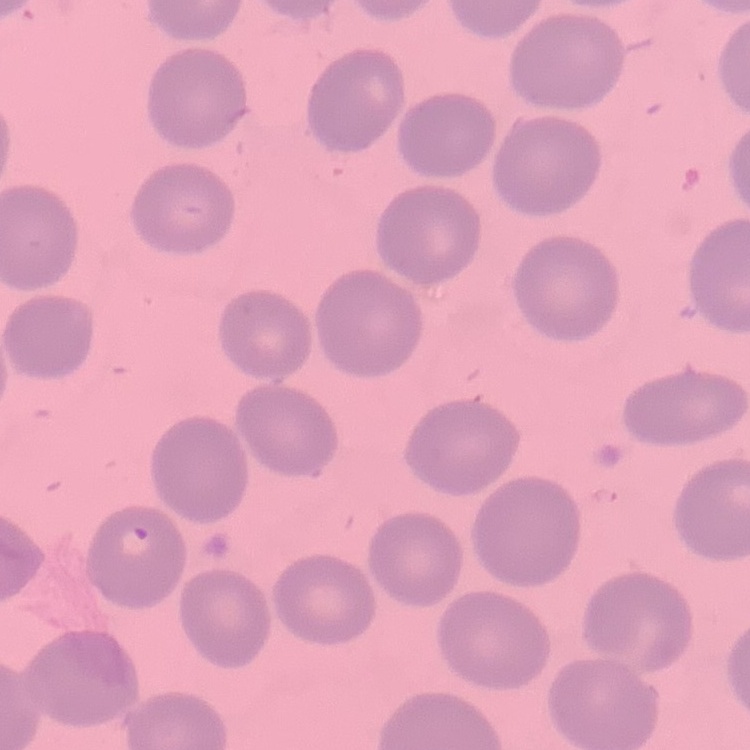

Summary:
  - Red blood cell morphology: no rouleaux formation
  - Stain: Field's or Giemsa
  - Image type: one tile cut from a larger photomicrograph
  - Preparation: thin blood film